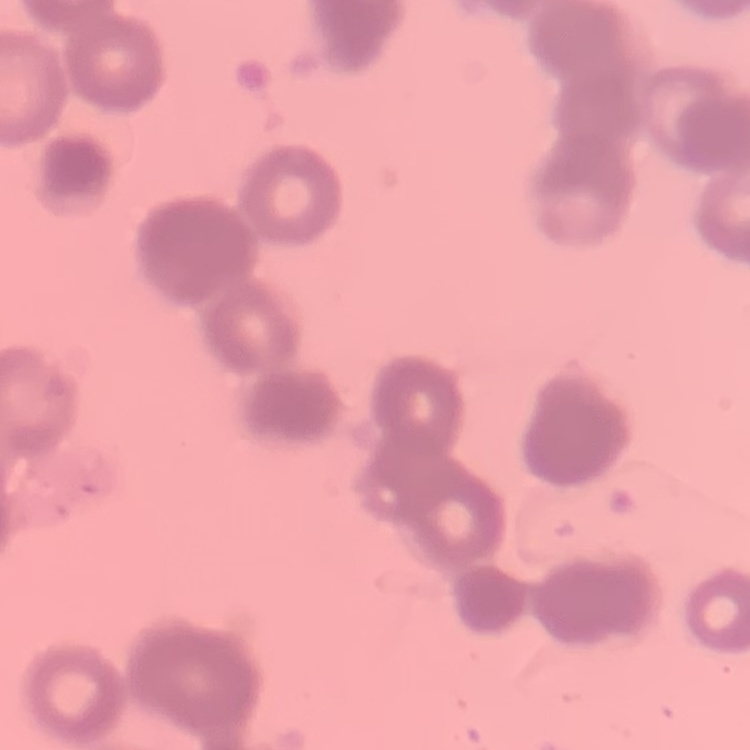

erythrocyte morphology = rouleaux formation
preparation = thin peripheral smear
image type = one tile cut from a larger photomicrograph
stain = Field's or Giemsa